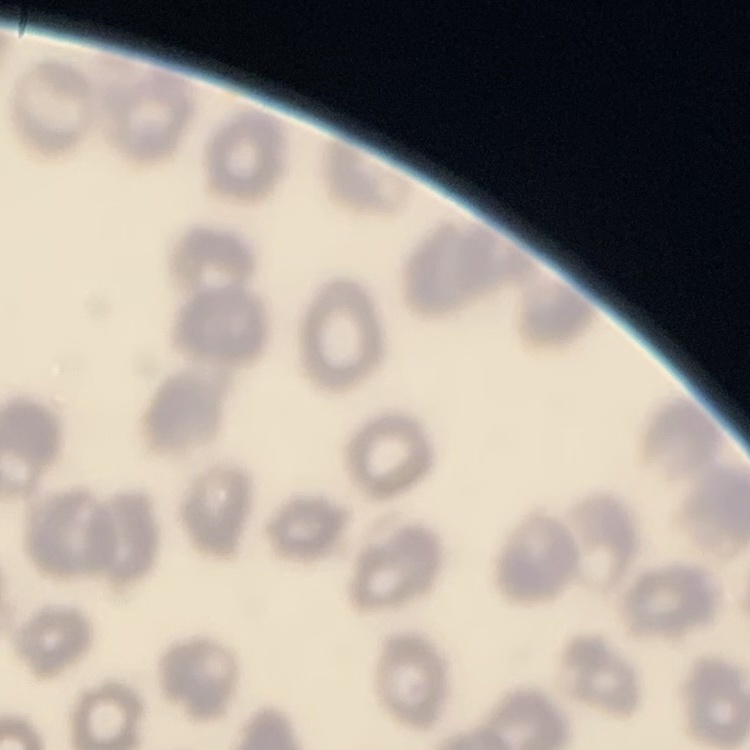

Summary:
  - Red blood cell morphology: no rouleaux formation
  - Image type: square crop of a larger photomicrograph
  - Stain: Field's or Giemsa
  - Preparation: thin blood smear